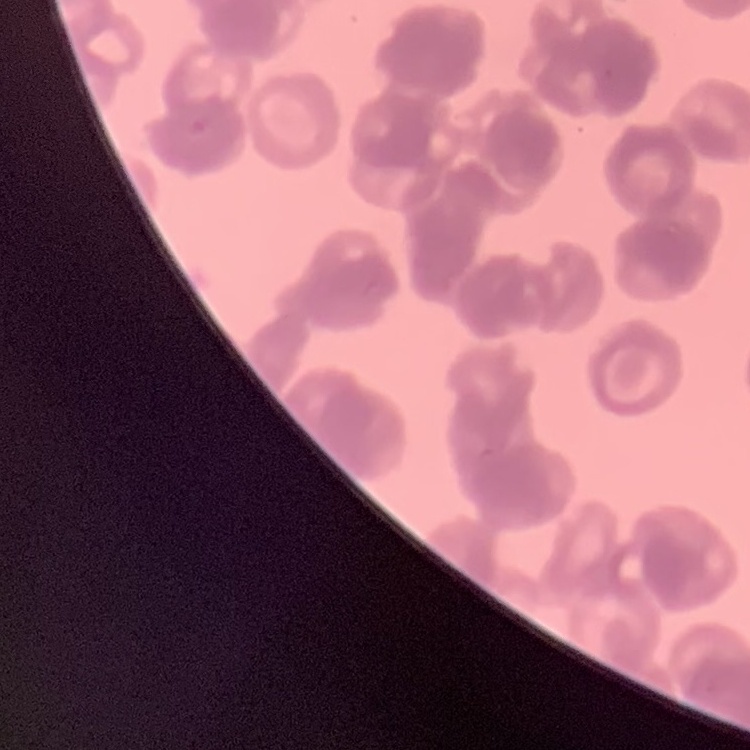
Summary:
  - Erythrocyte morphology: rouleaux formation
  - Preparation: thin blood film
  - Stain: Field's or Giemsa
  - Image type: square crop of a larger photomicrograph